Assess this cell for malaria.
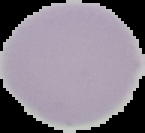
It is uninfected.

image size = 145×133 pixels
image type = segmented cell region with the area outside set to black
preparation = thin blood smear